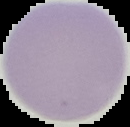

result = no Plasmodium parasites seen
image type = cell region segmented out of the field of view; surrounding area masked to black
image size = 130×127 pixels
preparation = thin blood smear